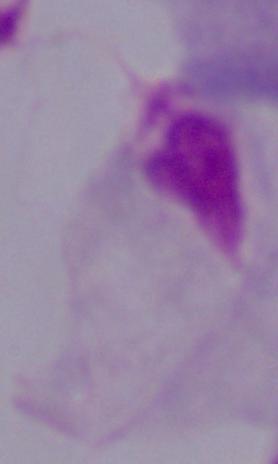

identification = trichomonad
modality = micrograph
magnification = 1000x